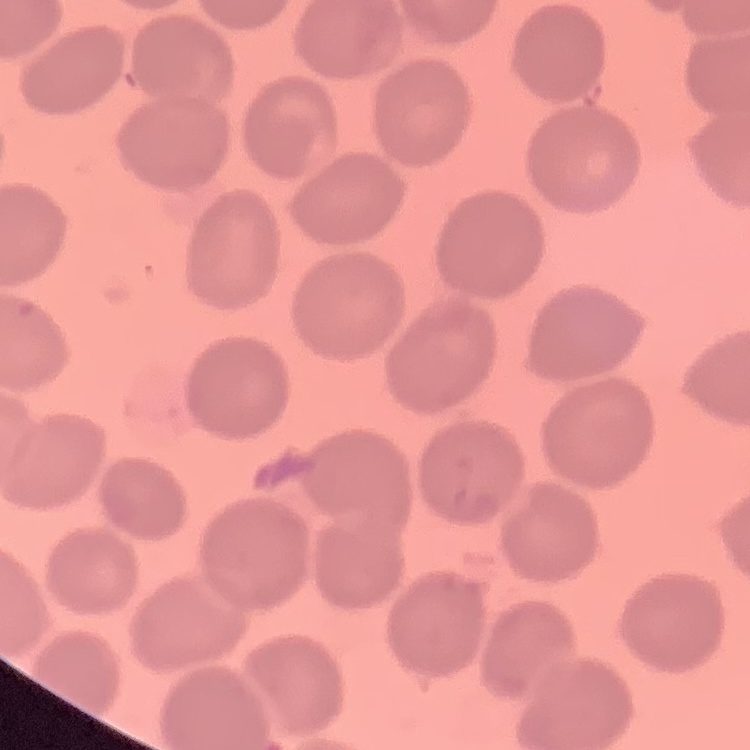

The red blood cells exhibit no rouleaux formation. Thin peripheral smear. Square crop of a larger photomicrograph. Stained with either Field's or Giemsa.